Comment on the morphology of the red blood cells.
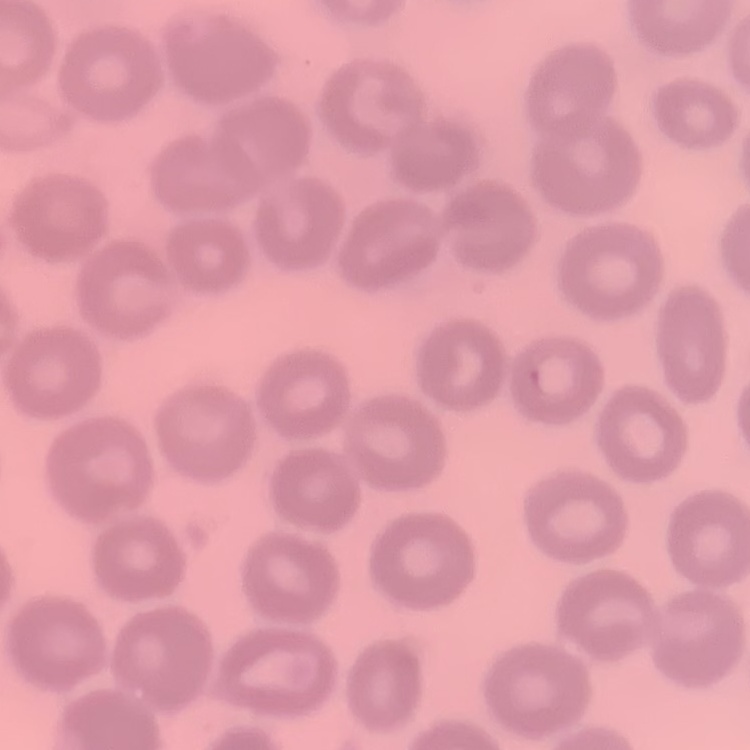
No rouleaux formation.

Summary:
  - Image type: square crop of a larger photomicrograph
  - Preparation: thin blood smear
  - Stain: Field's or Giemsa